Locate and identify every blood parasite.
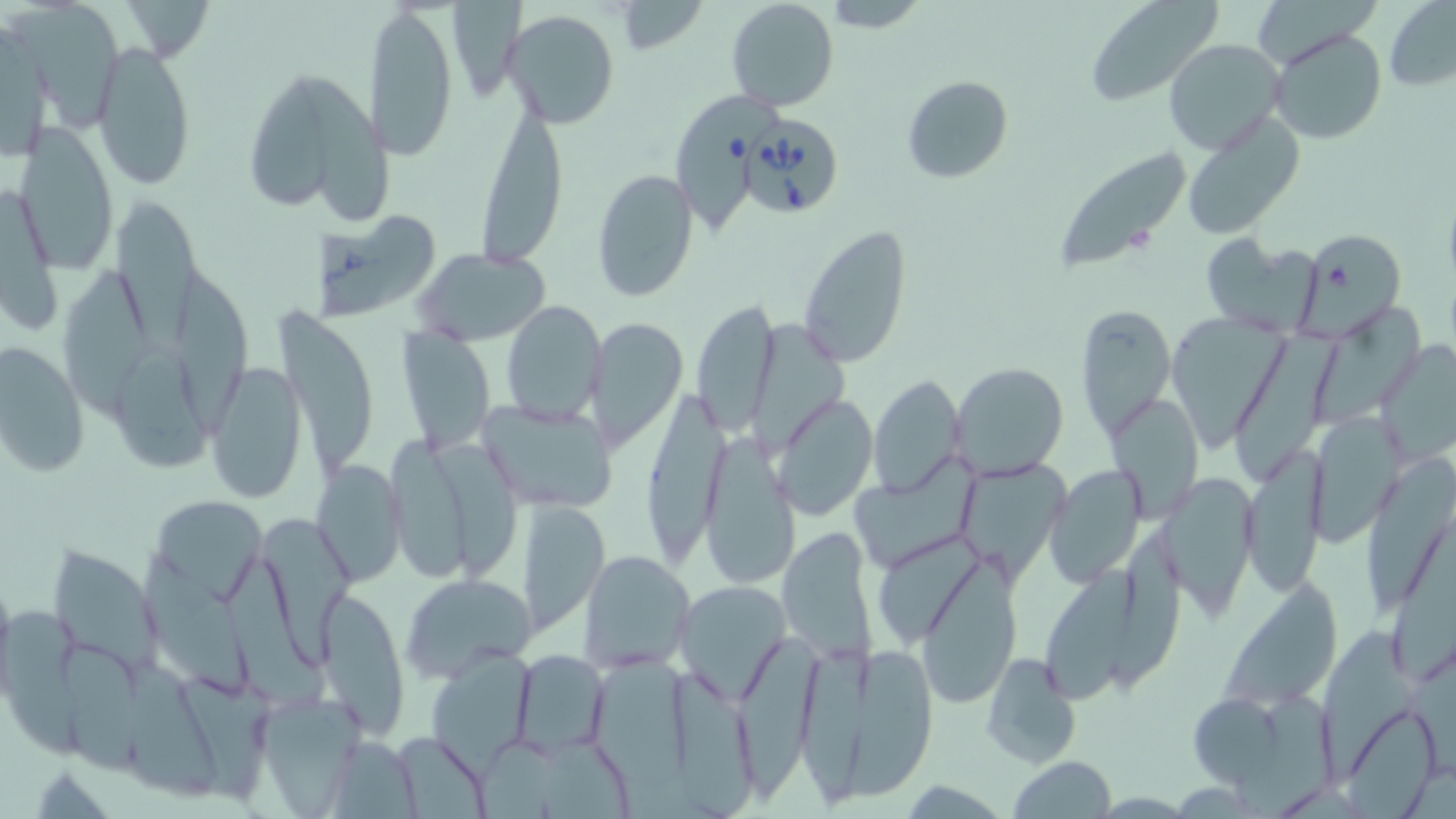
Approximate bounding boxes as (x1,y1)-(x2,y2) corner pairs in pixels.
Babesia divergens-infected red blood cells: (675,89)-(776,240), (740,114)-(845,219).
No Plasmodium falciparum, Plasmodium ovale, Plasmodium malariae, Plasmodium vivax, or Trypanosoma brucei observed.

Uninfected red blood cell locations: (120,0)-(213,65), (724,0)-(841,113), (823,0)-(929,30), (1084,0)-(1221,105), (453,1)-(525,102), (612,2)-(706,55), (1384,2)-(1455,92), (366,3)-(460,163), (11,4)-(124,132), (501,11)-(622,130), (0,21)-(56,156), (1267,28)-(1389,146), (91,37)-(196,191), (1162,38)-(1287,157), (902,74)-(1013,184), (250,75)-(331,212), (306,75)-(397,236), (477,99)-(568,265), (1181,114)-(1306,238), (12,130)-(118,272), (1048,146)-(1190,273), (592,169)-(698,302), (0,187)-(64,332), (111,196)-(203,354), (315,203)-(429,322), (797,223)-(913,369), (1300,228)-(1406,334), (1199,232)-(1323,332), (413,246)-(552,344), (63,263)-(155,421), (177,269)-(258,438), (690,299)-(779,437), (501,300)-(606,425), (1073,302)-(1177,446), (1316,304)-(1425,424), (274,306)-(380,470), (1166,314)-(1289,452), (583,317)-(688,454), (752,322)-(850,458), (1229,325)-(1350,487), (395,329)-(494,455), (1376,340)-(1456,464), (1,341)-(88,477), (113,346)-(218,472), (206,361)-(307,504), (951,362)-(1070,481), (869,374)-(966,496), (643,387)-(732,560), (1108,393)-(1204,520), (773,394)-(877,520), (477,395)-(617,511), (1306,413)-(1403,545), (381,432)-(469,586), (702,434)-(802,591), (435,440)-(521,575), (1241,448)-(1326,598), (851,452)-(989,564), (1365,458)-(1456,617), (314,462)-(407,586), (1044,465)-(1146,587), (959,468)-(1074,582), (1158,473)-(1258,616), (148,495)-(266,602), (517,500)-(608,634), (259,512)-(354,660), (777,527)-(878,665), (1390,527)-(1456,684), (47,546)-(163,675), (579,550)-(698,674), (141,551)-(254,697), (912,557)-(1022,706), (1044,559)-(1140,703), (225,563)-(330,708), (1216,571)-(1344,711), (400,574)-(537,681), (677,581)-(792,699), (321,587)-(408,734), (0,613)-(90,756), (1322,627)-(1412,775), (737,634)-(814,800), (52,637)-(148,780), (844,639)-(937,801), (806,646)-(865,816), (125,650)-(225,804), (512,650)-(610,755), (429,651)-(535,769), (981,653)-(1079,770), (595,658)-(694,794), (670,671)-(758,819), (176,675)-(275,801), (246,692)-(365,813), (1188,693)-(1286,786), (1230,694)-(1340,818), (1345,708)-(1439,819), (391,731)-(493,817), (544,731)-(630,819), (325,735)-(422,819), (478,737)-(559,819), (1009,757)-(1117,819), (901,779)-(1009,815). Slide-level diagnosis: Babesia divergens. Light microscopy. One field of a larger specimen. Image is 1456×819 pixels. May-Grünwald-Giemsa-stained preparation. Thin blood film. 1000x magnification.